Outline each blood parasite and name the species.
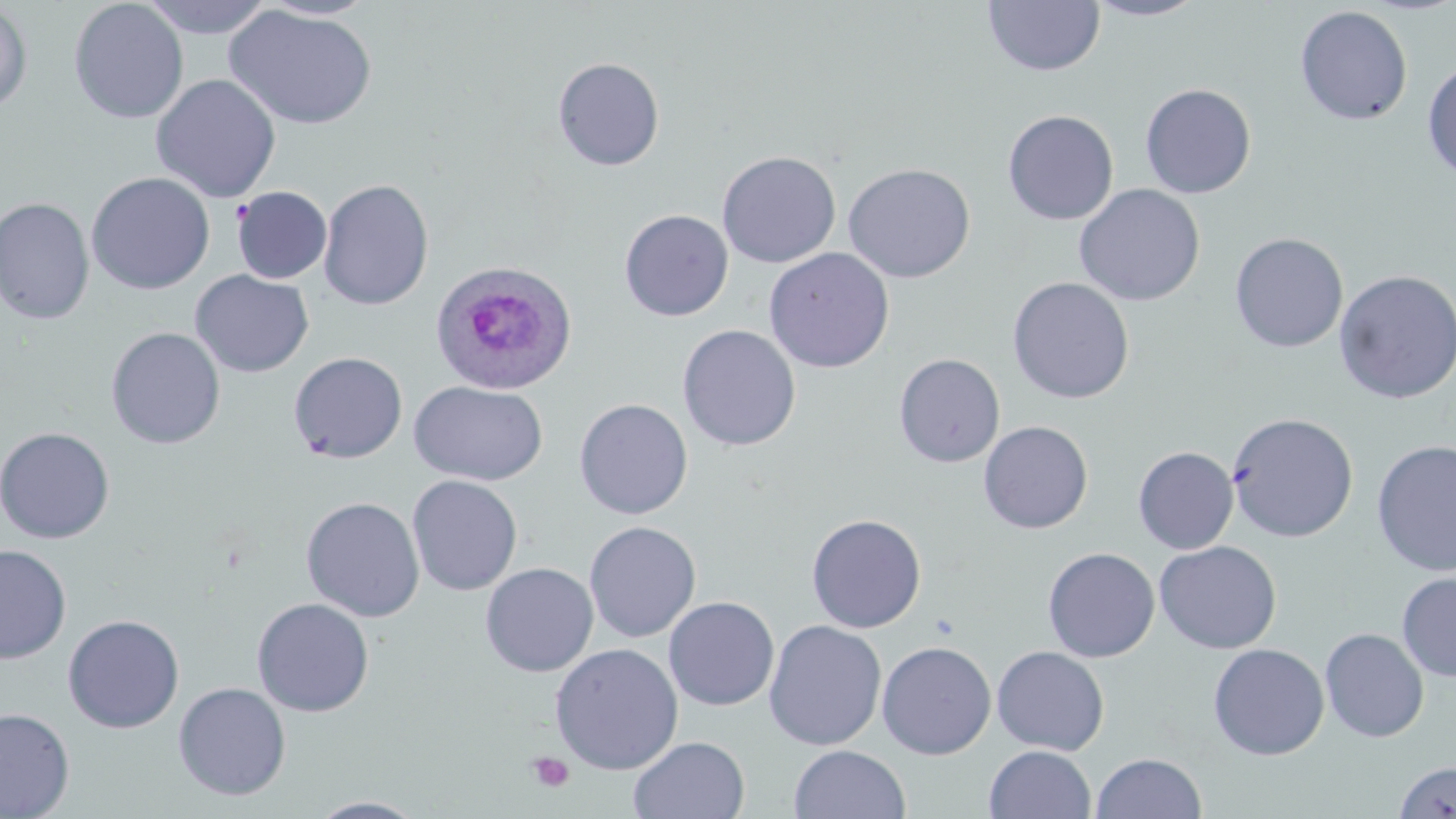
Approximate bounding boxes as (x1,y1)-(x2,y2) corner pairs in pixels.
Plasmodium ovale-infected red blood cells: (429,258)-(578,396).
No Plasmodium falciparum, Plasmodium malariae, Plasmodium vivax, Babesia divergens, or Trypanosoma brucei observed.

slide-level diagnosis = Plasmodium ovale
stain = May-Grünwald-Giemsa
platelet locations = approximate bounding boxes as (x1,y1)-(x2,y2) corner pairs in pixels: (527,751)-(575,793)
uninfected red blood cell locations = approximate bounding boxes as (x1,y1)-(x2,y2) corner pairs in pixels: (69,0)-(189,124), (139,0)-(275,39), (1084,0)-(1210,21), (256,1)-(379,21), (983,1)-(1105,77), (0,2)-(33,114), (224,4)-(378,130), (1294,5)-(1413,126), (552,57)-(665,171), (1422,59)-(1456,183), (151,74)-(282,203), (1139,83)-(1257,198), (1002,110)-(1119,226), (717,151)-(841,268), (842,163)-(976,283), (86,172)-(215,295), (318,179)-(434,310), (1074,184)-(1205,306), (232,187)-(332,284), (0,197)-(95,324), (619,209)-(734,321), (1229,233)-(1348,353), (763,247)-(895,373), (1333,269)-(1456,405), (191,270)-(314,378), (1007,277)-(1135,404), (678,324)-(801,451), (106,327)-(226,449), (288,351)-(408,464), (894,353)-(1005,468), (409,380)-(548,486), (574,398)-(693,519), (1226,412)-(1359,542), (978,421)-(1093,534), (0,426)-(115,543), (1371,439)-(1456,577), (1133,446)-(1238,554), (407,475)-(522,595), (301,497)-(425,622), (806,513)-(926,633), (583,521)-(701,642), (1154,541)-(1282,654), (0,544)-(71,663), (1043,547)-(1160,663), (480,563)-(599,677), (1396,572)-(1456,682), (663,597)-(780,710), (252,598)-(374,717), (63,614)-(184,734), (764,620)-(887,751), (1320,628)-(1429,742), (876,640)-(996,760), (549,643)-(684,775), (1208,643)-(1330,760), (991,646)-(1110,755), (173,682)-(291,800), (0,707)-(75,818), (628,735)-(750,819), (789,745)-(911,819), (984,745)-(1096,819), (1091,752)-(1206,819), (1393,761)-(1456,818), (308,797)-(428,818)
modality = optical microscopy
field of view = single
preparation = thin blood film
magnification = 1000x
image size = 1456×819 pixels